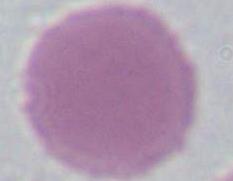

Photomicrograph. An erythrocyte is shown. Captured at 1000x magnification.